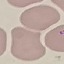
Summary:
  - Malaria status: uninfected
  - Stain: Giemsa
  - Preparation: thin blood smear
  - Capture: smartphone through the microscope eyepiece
  - Image type: cell patch, automatically extracted from a larger field of view and resized to 64 × 64 pixels